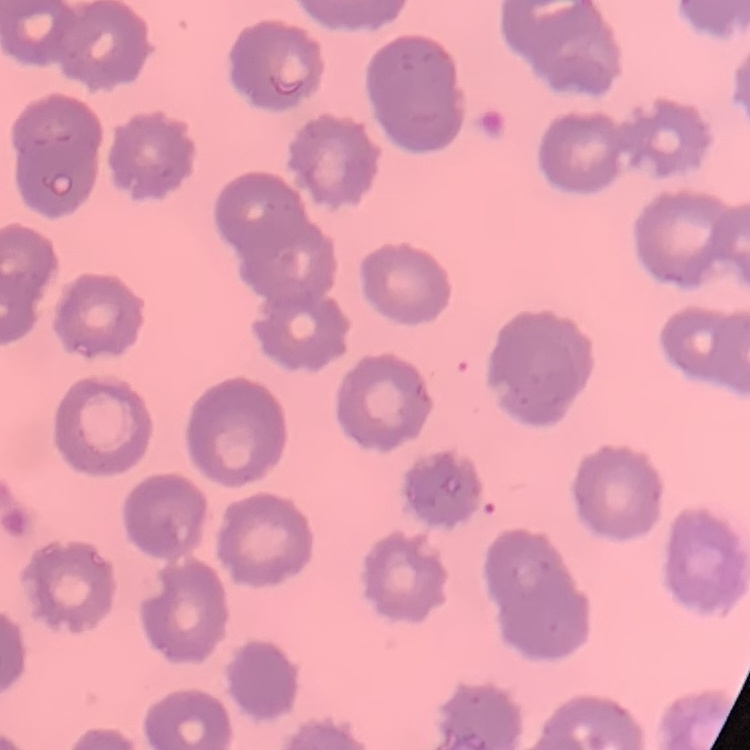
Summary:
  - Erythrocyte morphology: no rouleaux formation
  - Preparation: thin blood film
  - Stain: Field's or Giemsa
  - Image type: square crop of a larger photomicrograph